Give the preparation type.
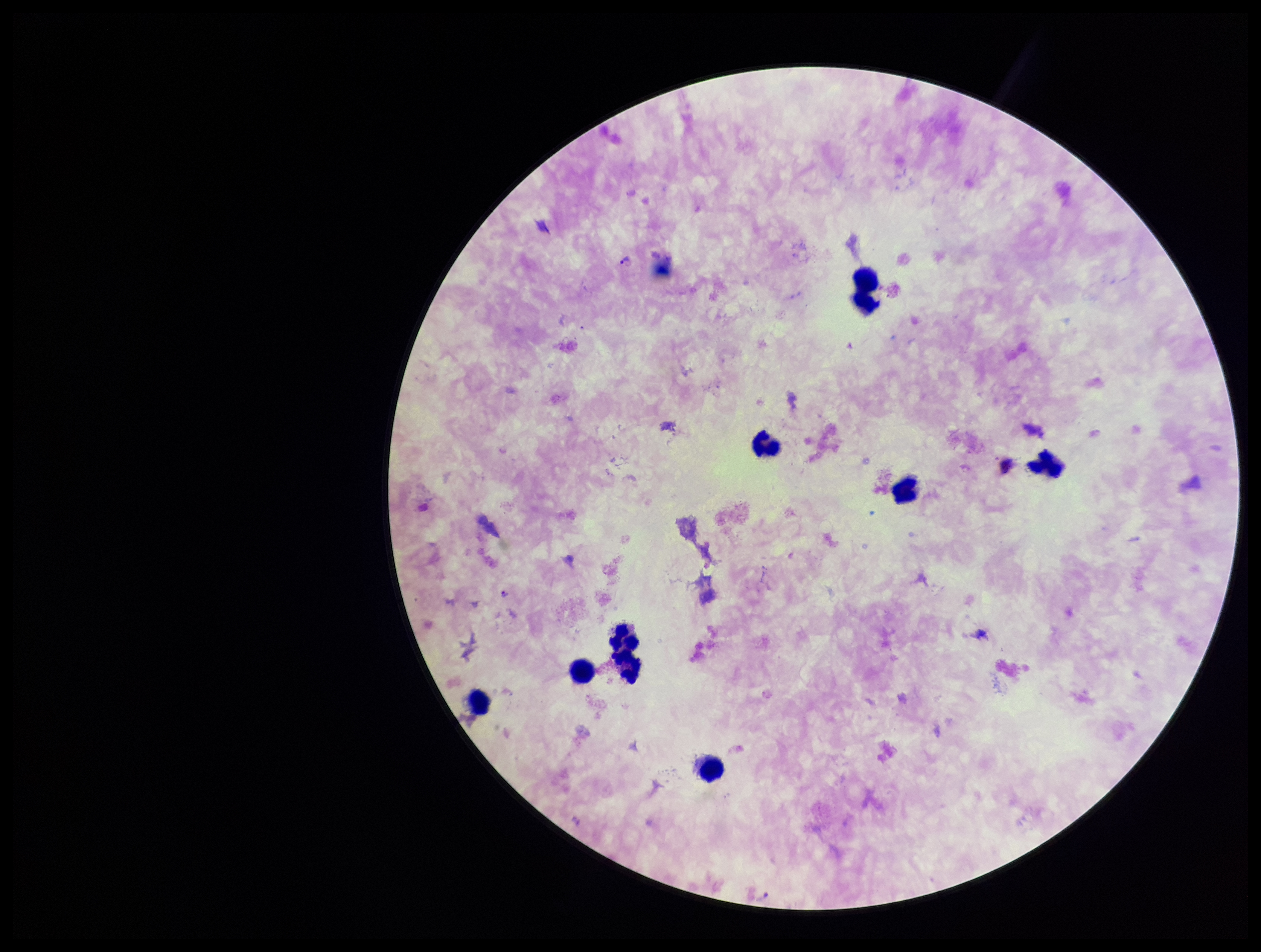
Thick.

image size = 1261×952 pixels
parasite count = 1
patient malaria status = positive
capture = smartphone photograph through the microscope eyepiece
field of view = one from this slide
leukocyte count = 9
Plasmodium parasites = seen
stain = Giemsa
species reported for this patient = Plasmodium falciparum